Assess this cell for malaria.
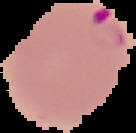

Parasitized.

Summary:
  - Preparation: thin blood film
  - Image type: cell region segmented out of the field of view; surrounding area masked to black
  - Image size: 136×133 pixels